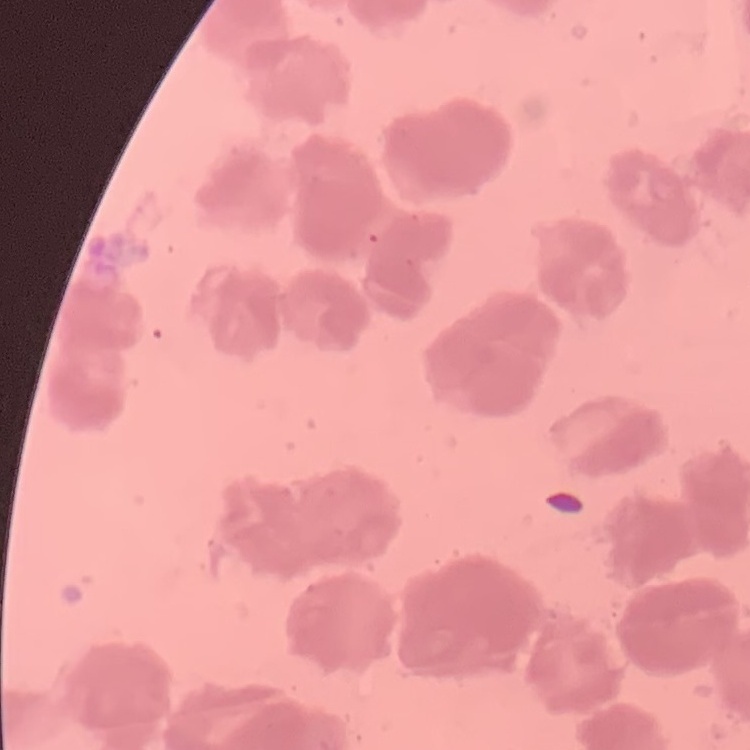
Summary:
  - Erythrocyte morphology: rouleaux formation
  - Image type: square crop of a larger photomicrograph
  - Stain: Field's or Giemsa
  - Preparation: thin blood smear